Identify the parasite.
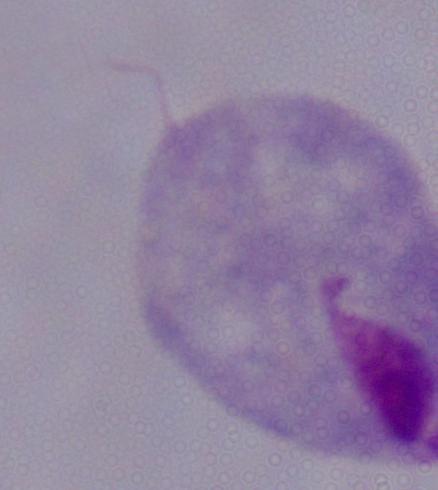

A trichomonad.

modality: photomicrograph
magnification: 1000x